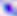
{
  "modality": "photomicrograph",
  "identification": "Toxoplasma gondii",
  "magnification": "400x"
}